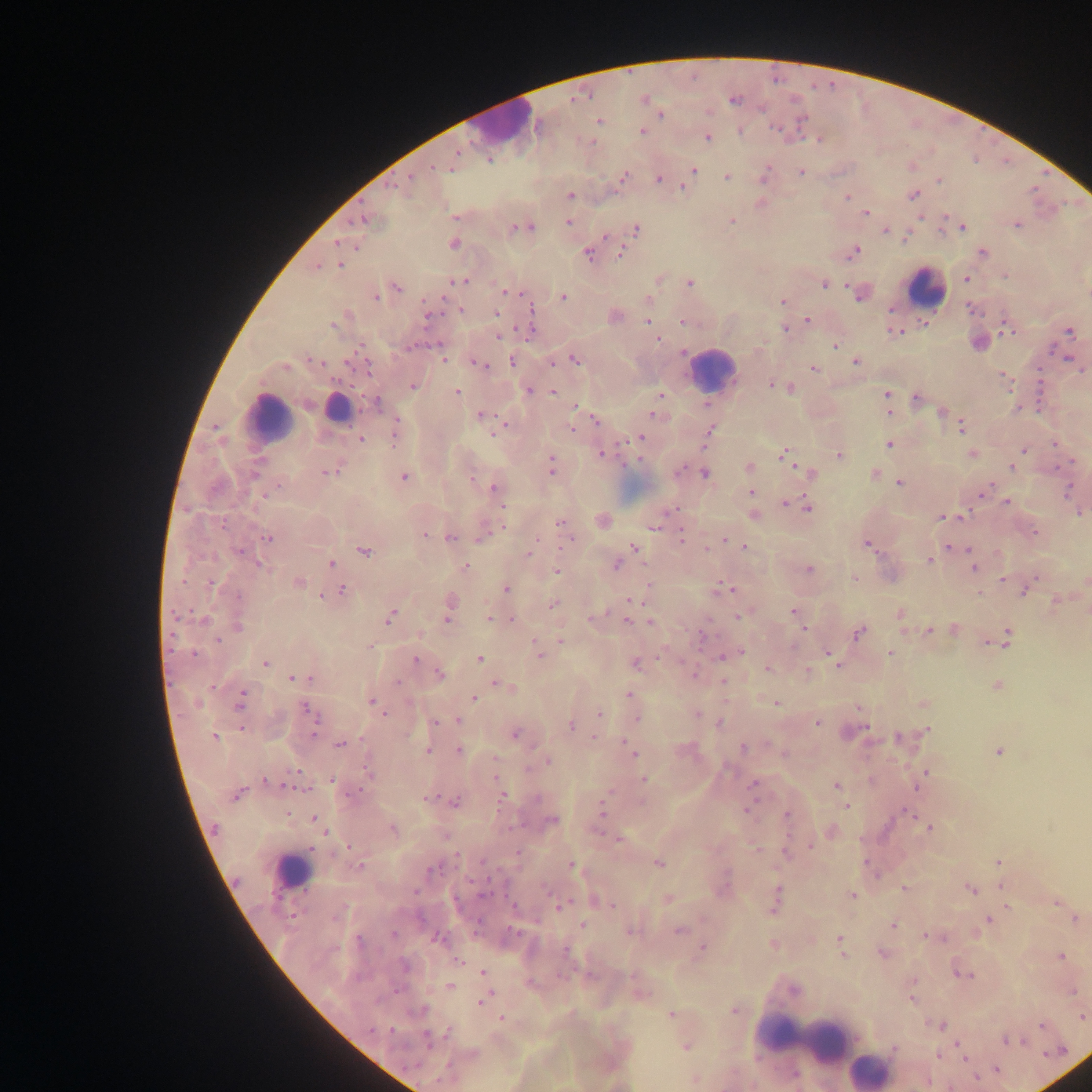
Approximate centers as [x, y] in pixels.
Summary:
  - Leukocyte locations: [506, 124], [926, 288], [712, 368], [336, 406], [271, 417], [291, 871], [801, 1038], [868, 1070]
  - Plasmodium parasite locations: [735, 100], [661, 114], [599, 120], [776, 130], [740, 131], [642, 132], [708, 137], [819, 140], [458, 153], [489, 160], [433, 167], [694, 170], [801, 172], [624, 176], [764, 176], [727, 177], [411, 178], [659, 178], [939, 179], [393, 186], [684, 188], [914, 195], [571, 196], [846, 197], [866, 212], [455, 217], [364, 220], [731, 221], [569, 223], [1017, 225], [526, 227], [963, 227], [515, 228], [636, 230], [886, 232], [337, 242], [453, 244], [621, 252], [854, 252], [588, 253], [982, 253], [340, 265], [318, 267], [966, 278], [461, 280], [690, 283], [824, 285], [397, 288], [506, 292], [858, 294], [564, 297], [376, 298], [783, 301], [891, 309], [459, 310], [532, 310], [497, 314], [428, 316], [807, 320], [647, 321], [682, 322], [333, 325], [785, 328], [1007, 328], [1070, 332], [895, 333], [499, 336], [657, 340], [835, 346], [410, 347], [683, 353], [443, 358], [575, 360], [314, 361], [512, 361], [856, 362], [552, 363], [478, 364], [368, 366], [285, 367], [814, 368], [771, 385], [413, 387], [790, 389], [529, 390], [457, 391], [552, 391], [660, 394], [886, 394], [918, 397], [888, 403], [376, 404], [577, 406], [889, 412], [942, 412], [653, 414], [480, 416], [596, 420], [503, 427], [961, 427], [572, 430], [709, 432], [394, 433], [639, 438], [361, 439], [889, 444], [1055, 444], [1023, 451], [785, 453], [603, 455], [972, 455], [839, 456], [551, 466], [1012, 467], [749, 468], [255, 471], [328, 471], [705, 473], [810, 473], [875, 473], [405, 478], [472, 478], [900, 483], [494, 488], [985, 489], [1068, 490], [752, 492], [1006, 503], [785, 504], [502, 506], [808, 508], [1080, 513], [755, 516], [958, 516], [942, 517], [603, 520], [223, 523], [561, 523], [655, 525], [1034, 532], [426, 535], [682, 536], [483, 537], [267, 538], [451, 538], [570, 539], [726, 540], [744, 546], [869, 546], [635, 547], [949, 547], [706, 549], [364, 551], [530, 551], [239, 552], [930, 560], [331, 563], [261, 565], [617, 565], [973, 566], [465, 567], [808, 569], [557, 571], [854, 579], [1003, 580], [1086, 581], [299, 582], [210, 583], [506, 589], [725, 589], [342, 591], [1024, 592], [321, 596], [237, 597], [632, 600], [1057, 601], [450, 604], [553, 605], [1087, 609], [794, 613], [901, 614], [390, 616], [488, 616], [593, 617], [739, 617], [447, 619], [493, 619], [203, 620], [510, 620], [627, 620], [651, 622], [238, 626], [803, 628], [955, 630], [929, 631], [859, 633], [703, 635], [1006, 639], [217, 641], [561, 641], [370, 647], [741, 651], [890, 653], [193, 654], [539, 655], [829, 655], [722, 657], [479, 659], [833, 659], [415, 660], [265, 663], [636, 665], [767, 668], [808, 670], [440, 674], [693, 675], [293, 678], [723, 681], [397, 682], [498, 683], [997, 686], [629, 695], [473, 697], [240, 701], [372, 702], [777, 703], [379, 708], [306, 709], [383, 713], [599, 714], [697, 714], [636, 717], [313, 718], [456, 720], [720, 722], [435, 723], [818, 723], [571, 726], [242, 729], [315, 730], [927, 730], [515, 735], [214, 737], [594, 738], [898, 738], [340, 744], [742, 748], [458, 750], [427, 751], [998, 751], [632, 752], [496, 759], [548, 761], [368, 771], [926, 772], [644, 779], [332, 780], [267, 781], [753, 786], [837, 786], [238, 794], [502, 797], [427, 799], [537, 799], [455, 802], [846, 807], [603, 810], [747, 811], [907, 812], [787, 814], [315, 819], [552, 820], [929, 828], [215, 829], [393, 829], [325, 830], [618, 840], [349, 846], [811, 846], [755, 849], [786, 853], [482, 861], [867, 862], [998, 862], [659, 863], [572, 866], [360, 867], [433, 869], [1002, 886], [905, 888], [970, 889], [484, 893], [852, 895], [777, 897], [668, 899], [1057, 902], [613, 905], [560, 906], [1007, 906], [1076, 919], [989, 920], [583, 925], [893, 925], [631, 931], [679, 931], [514, 932], [394, 935], [927, 936], [935, 936], [439, 939], [840, 940], [773, 944], [702, 948], [566, 950], [842, 954], [882, 954], [1061, 956], [458, 962], [483, 972], [963, 975], [530, 983], [451, 986], [794, 990], [1072, 991], [912, 998], [481, 1002], [421, 1010], [734, 1011], [672, 1015], [1082, 1017], [501, 1018], [939, 1025], [1041, 1025], [371, 1030], [391, 1031], [449, 1033], [428, 1037], [1007, 1040], [685, 1047], [895, 1049], [961, 1050], [937, 1056], [997, 1070], [795, 1073], [695, 1079]
  - Field of view: single
  - Country: Ghana
  - Preparation: thick blood smear
  - Capture: mobile-phone photograph through a microscope
  - Image size: 1092×1092 pixels